Name the cell type shown.
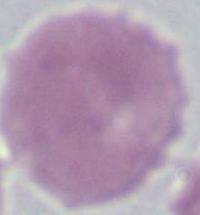
An erythrocyte.

modality = micrograph
magnification = 1000x